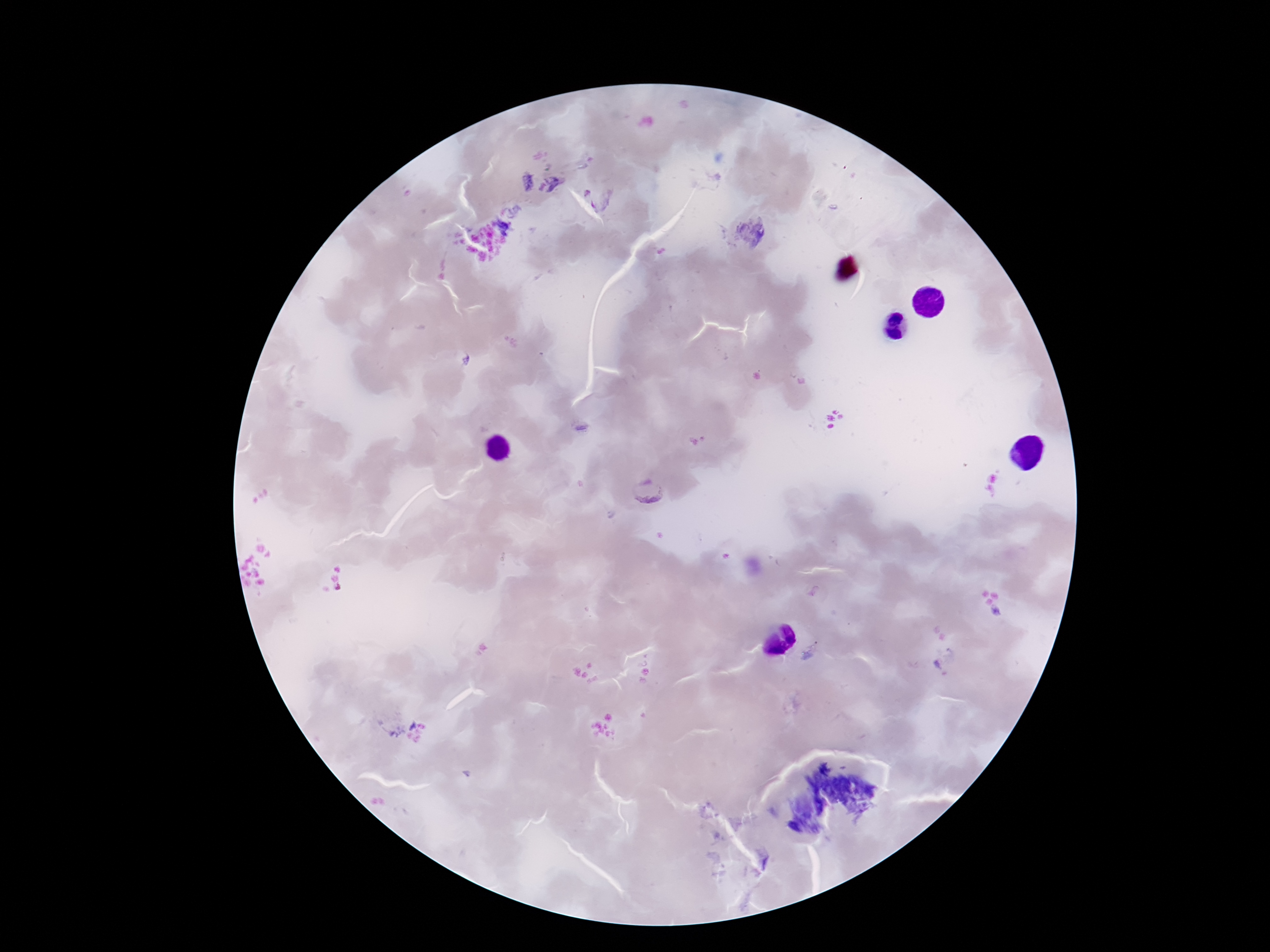
Approximate centers as {x, y} in pixels.
Summary:
  - Plasmodium parasite locations: {598, 198}, {648, 491}
  - Field of view: single
  - Preparation: thick blood smear
  - Patient malaria status: positive
  - Magnification: 100x
  - Image size: 1270×952 pixels
  - Capture: smartphone camera through the microscope eyepiece
  - Stain: Giemsa